Identify the parasite.
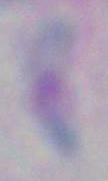

This is Toxoplasma gondii.

Summary:
  - Modality: micrograph
  - Magnification: 1000x